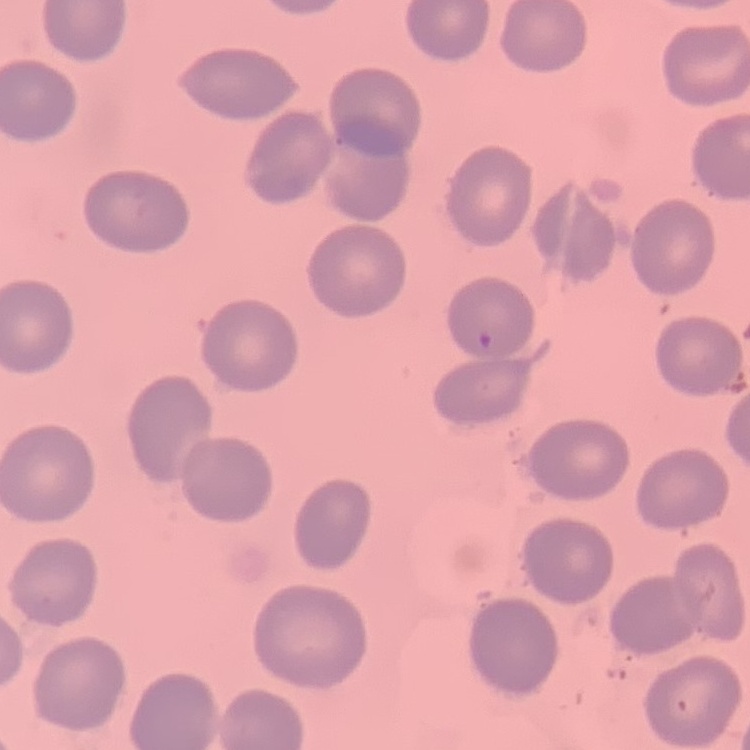
Summary:
  - Red blood cell morphology: no rouleaux formation
  - Stain: Field's or Giemsa
  - Preparation: thin blood film
  - Image type: square crop of a larger photomicrograph